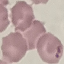

result: no malaria parasites seen
stain: Giemsa
preparation: thin blood film
image_type: automatically extracted cell patch, resized to 64 × 64 pixels
capture: smartphone camera at the microscope eyepiece